Outline platelets.
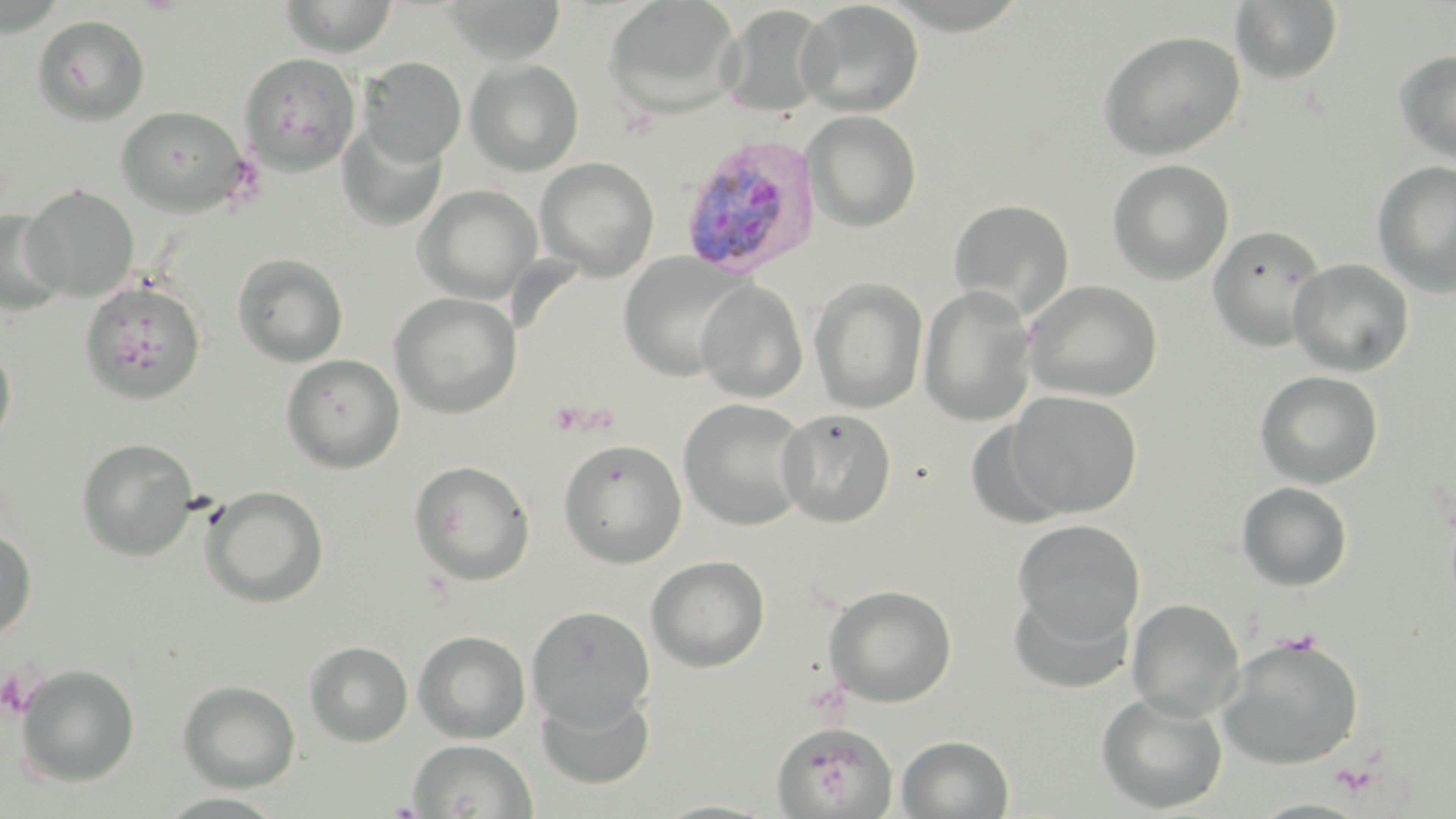

Approximate bounding boxes as named x1/y1/x2/y2 corners in pixels.
Platelets: (x1=547, y1=399, x2=605, y2=437), (x1=1278, y1=629, x2=1322, y2=656).

Summary:
  - Uninfected red blood cell locations: (x1=278, y1=0, x2=399, y2=58), (x1=441, y1=0, x2=567, y2=64), (x1=603, y1=0, x2=743, y2=119), (x1=0, y1=1, x2=71, y2=38), (x1=796, y1=1, x2=924, y2=117), (x1=1230, y1=1, x2=1344, y2=85), (x1=718, y1=4, x2=833, y2=118), (x1=31, y1=15, x2=150, y2=126), (x1=1096, y1=30, x2=1247, y2=161), (x1=1393, y1=48, x2=1456, y2=165), (x1=239, y1=53, x2=362, y2=176), (x1=358, y1=56, x2=467, y2=166), (x1=465, y1=59, x2=584, y2=176), (x1=116, y1=106, x2=249, y2=216), (x1=803, y1=110, x2=922, y2=232), (x1=336, y1=122, x2=448, y2=232), (x1=535, y1=157, x2=660, y2=280), (x1=1107, y1=159, x2=1235, y2=285), (x1=1372, y1=161, x2=1456, y2=297), (x1=22, y1=185, x2=139, y2=300), (x1=413, y1=185, x2=541, y2=303), (x1=949, y1=199, x2=1075, y2=318), (x1=0, y1=210, x2=67, y2=315), (x1=1208, y1=224, x2=1327, y2=352), (x1=232, y1=252, x2=348, y2=367), (x1=617, y1=253, x2=751, y2=382), (x1=1288, y1=259, x2=1415, y2=377), (x1=810, y1=278, x2=928, y2=413), (x1=695, y1=279, x2=809, y2=403), (x1=1024, y1=280, x2=1163, y2=402), (x1=80, y1=281, x2=206, y2=404), (x1=918, y1=286, x2=1038, y2=427), (x1=389, y1=292, x2=521, y2=419), (x1=0, y1=343, x2=16, y2=452), (x1=281, y1=353, x2=405, y2=472), (x1=1254, y1=370, x2=1384, y2=489), (x1=1004, y1=390, x2=1143, y2=519), (x1=678, y1=398, x2=812, y2=531), (x1=777, y1=408, x2=897, y2=528), (x1=77, y1=438, x2=199, y2=561), (x1=558, y1=439, x2=687, y2=568), (x1=409, y1=460, x2=536, y2=585), (x1=1236, y1=481, x2=1354, y2=591), (x1=200, y1=485, x2=328, y2=608), (x1=1012, y1=519, x2=1146, y2=644), (x1=0, y1=531, x2=37, y2=639), (x1=646, y1=555, x2=770, y2=672), (x1=824, y1=584, x2=958, y2=708), (x1=1009, y1=587, x2=1135, y2=695), (x1=1126, y1=597, x2=1245, y2=719), (x1=526, y1=605, x2=655, y2=728), (x1=413, y1=631, x2=531, y2=743), (x1=1217, y1=635, x2=1365, y2=770), (x1=304, y1=641, x2=413, y2=747), (x1=15, y1=663, x2=140, y2=788), (x1=177, y1=680, x2=300, y2=792), (x1=536, y1=688, x2=655, y2=790), (x1=1095, y1=691, x2=1228, y2=814), (x1=771, y1=721, x2=897, y2=818), (x1=896, y1=734, x2=1014, y2=818), (x1=409, y1=739, x2=537, y2=818), (x1=650, y1=799, x2=785, y2=818)
  - Plasmodium vivax-infected red blood cell locations: (x1=678, y1=133, x2=820, y2=277)
  - Slide-level diagnosis: Plasmodium vivax
  - Stain: May-Grünwald-Giemsa
  - Field of view: single
  - Preparation: thin blood smear
  - Magnification: 1000x
  - Image size: 1456×819 pixels
  - Modality: optical microscopy